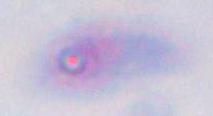
Summary:
  - Magnification: 1000x
  - Identification: Toxoplasma gondii
  - Modality: photomicrograph